Locate every blood parasite and identify its species.
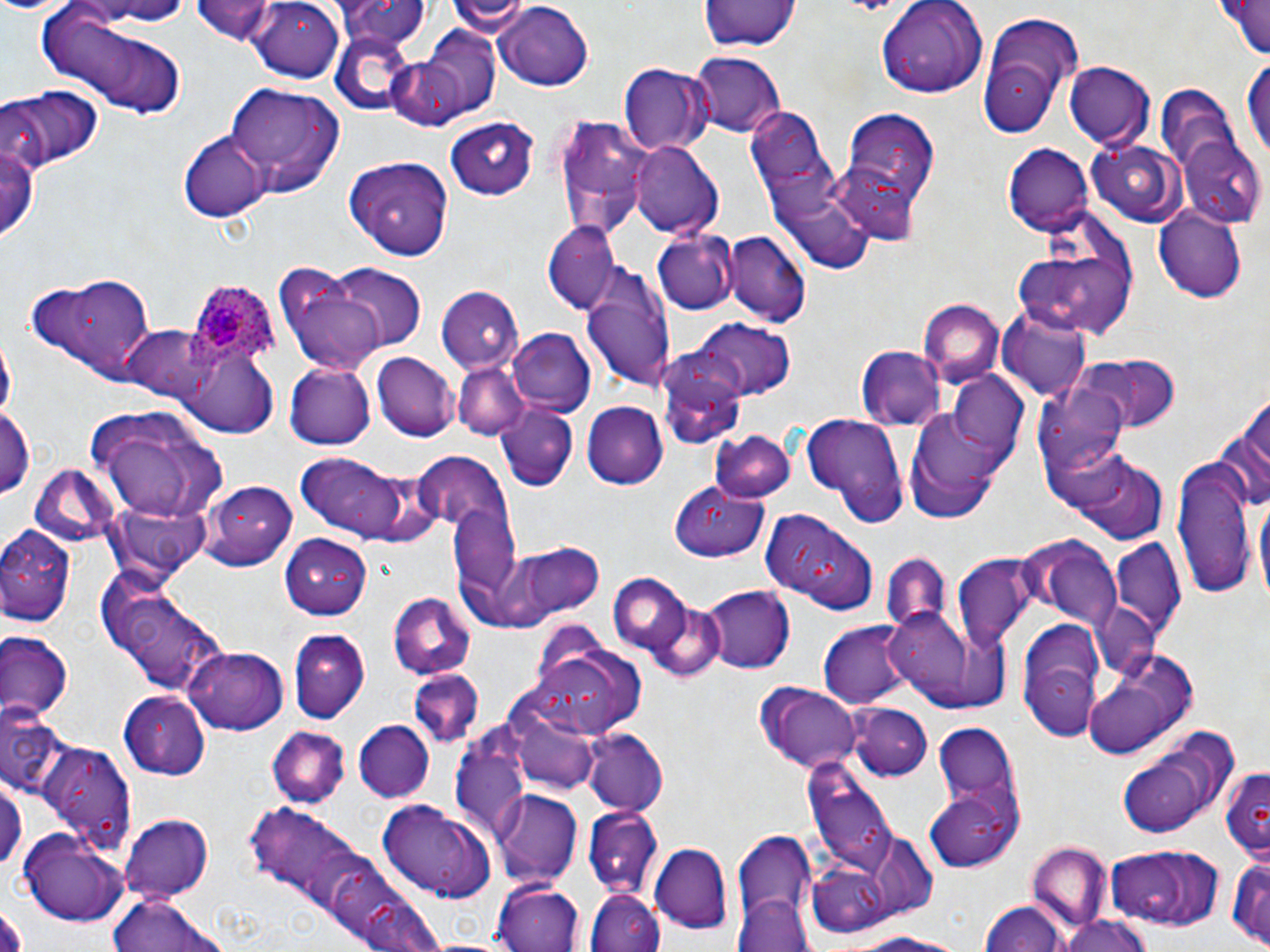
Approximate bounding boxes as (x1,y1)-(x2,y2) corner pairs in pixels.
Plasmodium ovale-infected red blood cells: (186,278)-(281,372).
No Plasmodium falciparum, Plasmodium malariae, Plasmodium vivax, Babesia divergens, or Trypanosoma brucei observed.

slide-level diagnosis = Plasmodium ovale
stain = May-Grünwald-Giemsa
magnification = 1000x
modality = optical microscopy
preparation = thin blood film
image size = 1270×952 pixels
uninfected red blood cell locations = approximate bounding boxes as (x1,y1)-(x2,y2) corner pairs in pixels: (80,0)-(197,25), (192,0)-(283,42), (334,0)-(431,50), (447,0)-(531,36), (1210,0)-(1270,60), (703,1)-(798,54), (242,2)-(345,79), (877,2)-(983,99), (493,3)-(596,90), (38,8)-(190,120), (980,13)-(1091,132), (329,30)-(420,115), (388,30)-(503,126), (688,50)-(787,137), (617,61)-(715,154), (1065,61)-(1154,150), (1242,63)-(1269,164), (223,80)-(345,197), (1154,84)-(1246,200), (5,85)-(102,171), (745,108)-(831,198), (843,109)-(942,206), (550,110)-(652,241), (445,116)-(541,200), (0,130)-(40,247), (178,132)-(269,223), (1179,133)-(1268,224), (1086,139)-(1185,226), (630,140)-(722,238), (1005,144)-(1093,236), (339,158)-(457,261), (830,164)-(924,246), (772,199)-(879,282), (1153,207)-(1246,301), (544,221)-(619,314), (726,229)-(811,326), (655,231)-(737,316), (1011,235)-(1138,340), (327,265)-(424,352), (581,265)-(678,394), (24,271)-(163,382), (282,273)-(387,375), (436,282)-(527,373), (918,300)-(1003,385), (998,310)-(1091,401), (686,320)-(797,402), (123,324)-(212,401), (507,328)-(594,414), (2,336)-(16,424), (856,346)-(942,431), (179,347)-(279,437), (1075,350)-(1182,433), (371,352)-(459,441), (453,362)-(531,441), (285,363)-(374,450), (1035,374)-(1132,484), (946,376)-(1031,464), (665,379)-(752,449), (1219,393)-(1270,518), (496,402)-(579,491), (582,402)-(669,488), (0,404)-(36,503), (85,405)-(227,525), (902,406)-(1008,521), (799,413)-(910,525), (713,428)-(795,502), (411,450)-(521,529), (295,452)-(419,542), (1174,454)-(1256,601), (1072,456)-(1167,543), (26,464)-(119,548), (202,479)-(299,574), (671,485)-(767,563), (1255,494)-(1269,606), (448,504)-(523,609), (761,511)-(879,615), (0,523)-(79,627), (280,532)-(372,618), (1109,536)-(1187,646), (1031,539)-(1121,630), (514,541)-(608,620), (881,553)-(949,637), (951,553)-(1040,651), (99,574)-(230,697), (609,574)-(695,658), (702,584)-(795,673), (388,592)-(476,680), (1092,604)-(1161,681), (885,607)-(995,710), (1016,617)-(1111,734), (820,620)-(909,709), (288,630)-(369,724), (0,632)-(72,723), (526,636)-(649,737), (185,647)-(289,735), (1082,654)-(1191,760), (405,672)-(486,749), (756,684)-(863,773), (119,691)-(211,779), (852,704)-(932,779), (0,711)-(73,803), (354,720)-(434,801), (517,720)-(598,792), (933,723)-(1020,814), (266,727)-(350,809), (1114,729)-(1238,842), (582,730)-(670,817), (41,741)-(135,849), (450,743)-(532,845), (806,761)-(898,879), (1218,765)-(1270,859), (0,768)-(26,878), (927,788)-(1023,869), (491,791)-(582,885), (379,797)-(498,900), (242,805)-(335,885), (583,810)-(664,898), (120,814)-(213,898), (20,829)-(129,926), (732,833)-(817,939), (1028,842)-(1109,926), (1107,843)-(1226,929), (649,845)-(732,933), (307,847)-(401,926), (1226,856)-(1269,947), (808,863)-(895,938), (492,880)-(583,952), (585,889)-(666,952), (109,894)-(224,952), (736,896)-(815,952), (361,897)-(444,952), (980,898)-(1069,951), (1056,913)-(1155,952), (851,930)-(975,951)
field of view = single